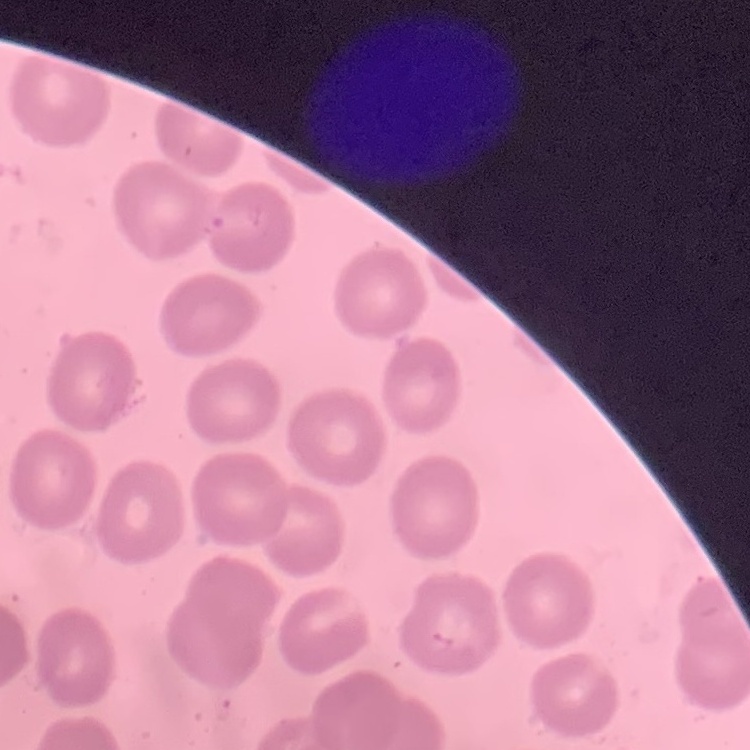
The red blood cells show no rouleaux formation. Square crop of a larger photomicrograph. Thin blood film. Field's or Giemsa stain.